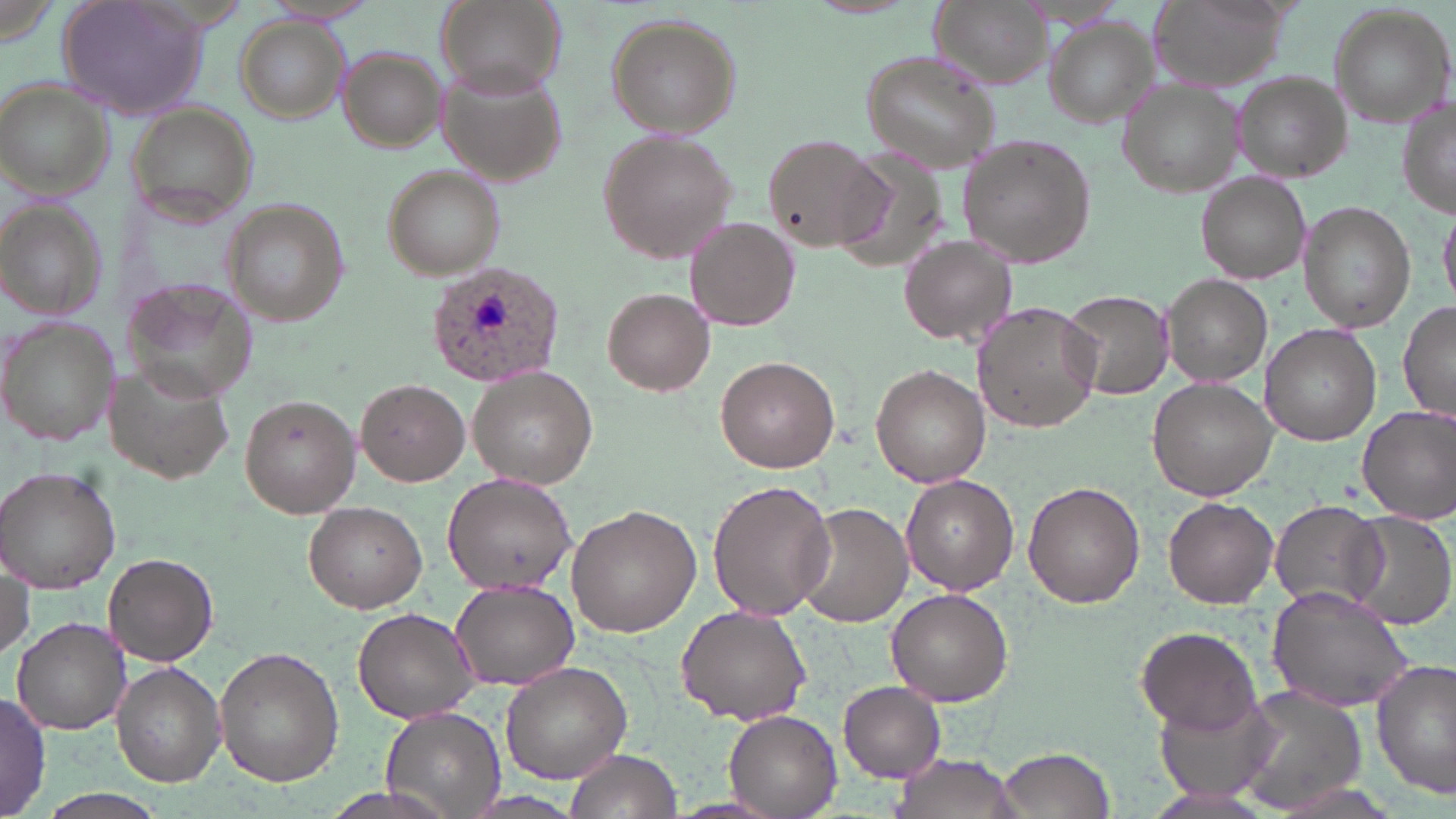

Summary:
  - Coordinate format: approximate bounding boxes as [x1, y1, x2, y2] in pixels
  - Plasmodium ovale-infected red blood cell locations: [426, 260, 567, 387]
  - Uninfected red blood cell locations: [59, 0, 209, 122], [437, 0, 565, 97], [928, 0, 1051, 89], [1145, 0, 1293, 92], [259, 1, 381, 26], [1328, 5, 1453, 129], [606, 13, 740, 136], [1046, 18, 1157, 125], [236, 19, 349, 123], [336, 47, 445, 152], [860, 50, 1001, 173], [439, 66, 569, 187], [1231, 73, 1351, 182], [0, 81, 117, 199], [1120, 81, 1242, 196], [1397, 95, 1456, 222], [124, 106, 259, 225], [598, 128, 740, 264], [958, 133, 1099, 268], [763, 134, 885, 251], [832, 145, 954, 269], [383, 167, 505, 277], [1196, 171, 1311, 285], [223, 201, 348, 325], [1301, 203, 1415, 331], [1440, 203, 1456, 307], [1, 205, 105, 322], [686, 218, 798, 330], [901, 234, 1017, 346], [1161, 273, 1272, 388], [121, 279, 261, 407], [603, 288, 715, 396], [1061, 288, 1176, 401], [973, 301, 1102, 431], [1399, 301, 1454, 428], [0, 316, 119, 448], [1262, 325, 1382, 445], [714, 355, 840, 473], [106, 363, 236, 484], [871, 364, 989, 487], [469, 367, 602, 490], [1148, 377, 1278, 499], [356, 378, 470, 486], [240, 394, 361, 517], [1357, 404, 1456, 523], [0, 466, 123, 593], [440, 471, 577, 593], [901, 474, 1018, 595], [707, 479, 835, 622], [1024, 480, 1146, 608], [1163, 497, 1279, 607], [303, 501, 427, 613], [1268, 502, 1388, 611], [798, 503, 913, 627], [567, 505, 700, 637], [1342, 510, 1455, 630], [102, 552, 218, 667], [0, 562, 33, 661], [450, 579, 580, 689], [1266, 585, 1415, 713], [886, 588, 1015, 707], [676, 605, 812, 724], [352, 607, 480, 724], [11, 618, 130, 734], [1137, 625, 1263, 733], [216, 647, 343, 787], [1370, 659, 1455, 800], [111, 662, 226, 786], [501, 662, 631, 783], [838, 682, 946, 781], [1233, 685, 1368, 813], [1153, 688, 1281, 801], [0, 692, 51, 818], [381, 707, 504, 818], [723, 708, 843, 816], [994, 746, 1117, 818], [564, 748, 681, 819], [892, 752, 1025, 819]
  - Slide-level diagnosis: Plasmodium ovale
  - Image size: 1456×819 pixels
  - Stain: May-Grünwald-Giemsa
  - Field of view: one of a larger specimen
  - Magnification: 1000x
  - Preparation: thin blood film
  - Modality: optical microscopy